Identify the blood parasite species.
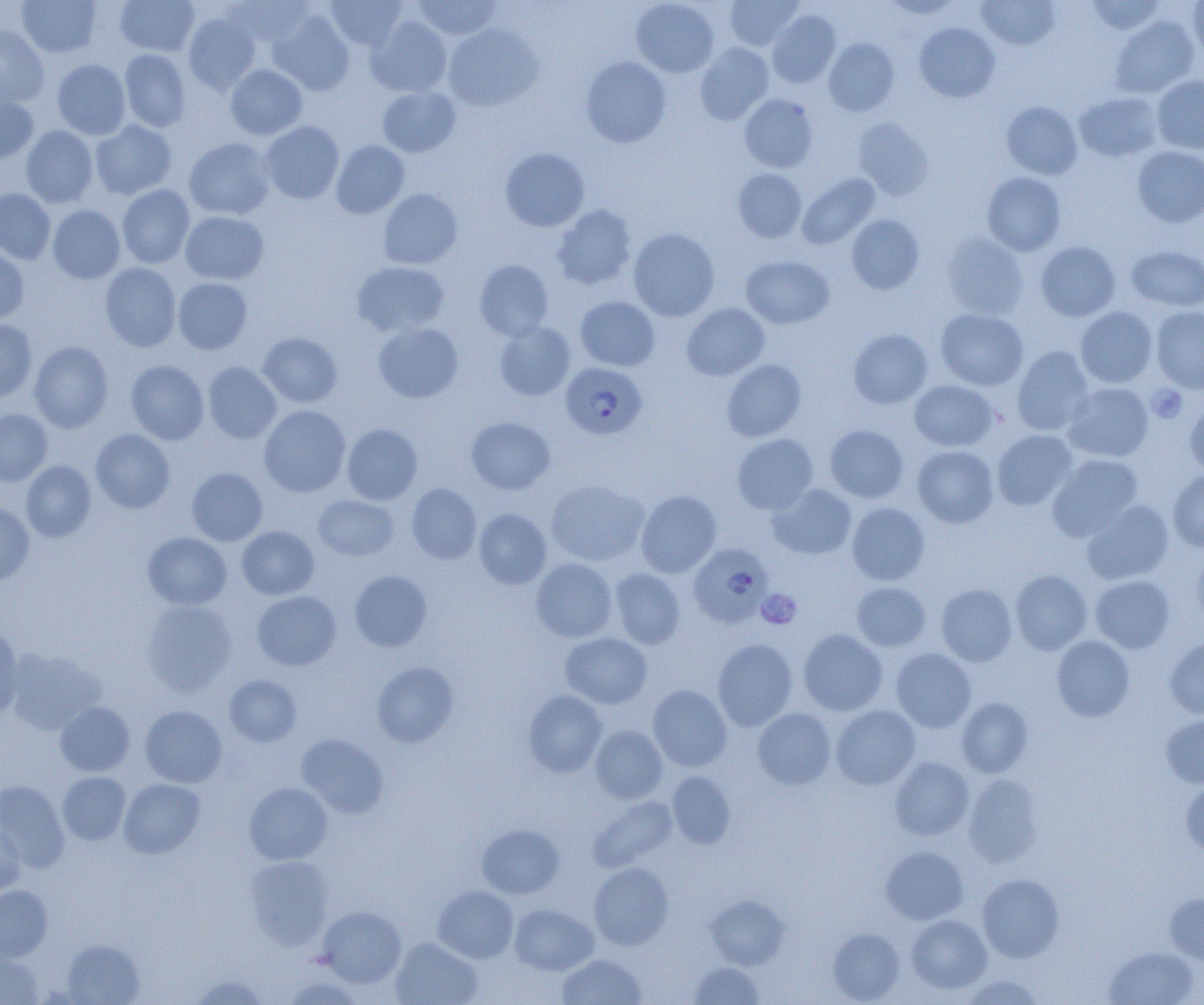
Plasmodium falciparum.

Approximate bounding boxes as (x1, y1, x2, y2) in pixels. Platelet locations: (1147, 384, 1187, 423), (757, 589, 802, 629). Plasmodium falciparum-infected red blood cell locations: (560, 362, 647, 439), (689, 543, 772, 627). Uninfected red blood cell locations: (17, 0, 101, 58), (115, 0, 199, 57), (225, 0, 313, 47), (325, 0, 408, 51), (631, 0, 719, 78), (724, 0, 804, 51), (1085, 0, 1168, 37), (1188, 0, 1204, 61), (413, 1, 503, 40), (882, 1, 964, 19), (976, 1, 1060, 50), (268, 9, 354, 96), (767, 10, 841, 87), (182, 13, 261, 94), (1109, 15, 1200, 99), (367, 16, 452, 97), (914, 22, 1000, 102), (443, 23, 543, 111), (0, 26, 49, 107), (824, 37, 899, 116), (694, 42, 774, 125), (119, 49, 191, 132), (581, 57, 671, 147), (52, 59, 131, 140), (225, 64, 307, 140), (1152, 75, 1204, 155), (377, 86, 460, 157), (1074, 91, 1165, 163), (0, 93, 38, 163), (740, 93, 818, 172), (1001, 101, 1083, 179), (852, 118, 934, 200), (90, 120, 177, 200), (259, 121, 344, 204), (21, 125, 98, 208), (183, 137, 275, 220), (331, 140, 409, 218), (1132, 146, 1204, 227), (500, 148, 590, 231), (733, 168, 806, 242), (982, 172, 1065, 255), (797, 174, 880, 249), (117, 184, 195, 268), (0, 188, 55, 264), (378, 188, 462, 270), (552, 204, 637, 290), (47, 205, 125, 284), (180, 211, 269, 285), (846, 214, 924, 294), (628, 228, 720, 321), (941, 232, 1029, 320), (1035, 241, 1121, 322), (0, 245, 30, 324), (1126, 245, 1204, 311), (741, 255, 834, 328), (475, 259, 553, 341), (352, 261, 449, 337), (100, 263, 181, 352), (173, 278, 252, 354), (575, 296, 660, 371), (682, 303, 769, 381), (1075, 306, 1158, 388), (1151, 306, 1204, 393), (935, 308, 1028, 391), (0, 319, 37, 402), (373, 322, 463, 403), (494, 323, 575, 401), (848, 329, 933, 409), (258, 333, 342, 407), (29, 341, 113, 432), (1012, 346, 1094, 435), (722, 359, 806, 442), (126, 360, 209, 445), (202, 361, 282, 444), (908, 380, 998, 452), (1063, 382, 1154, 462), (1184, 398, 1204, 478), (259, 405, 351, 497), (0, 408, 52, 486), (466, 417, 555, 494), (342, 423, 422, 505), (825, 425, 908, 503), (91, 428, 175, 513), (992, 430, 1077, 510), (733, 434, 818, 514), (912, 446, 998, 528), (1046, 454, 1143, 541), (21, 460, 96, 542), (187, 468, 267, 546), (1167, 470, 1204, 552), (546, 479, 649, 566), (407, 483, 482, 564), (768, 483, 857, 560), (636, 490, 721, 577), (313, 494, 399, 560), (1081, 499, 1174, 585), (0, 502, 35, 586), (846, 502, 930, 585), (473, 509, 552, 589), (236, 526, 319, 599), (143, 532, 232, 609), (1191, 547, 1204, 631), (530, 558, 617, 643), (609, 568, 685, 649), (349, 570, 432, 651), (1010, 570, 1092, 655), (1090, 575, 1175, 653), (851, 582, 932, 652), (936, 584, 1018, 667), (252, 591, 340, 670), (142, 600, 237, 696), (0, 623, 24, 720), (798, 629, 888, 716), (559, 632, 652, 709), (1052, 635, 1135, 722), (712, 638, 797, 731), (1164, 638, 1204, 719), (5, 648, 105, 734), (891, 648, 976, 732), (372, 661, 458, 747), (224, 675, 302, 746), (648, 685, 732, 771), (523, 690, 607, 777), (956, 697, 1033, 778), (55, 702, 134, 776), (140, 705, 227, 788), (830, 705, 921, 790), (752, 707, 836, 789), (1160, 714, 1204, 789), (590, 725, 667, 804), (296, 733, 388, 818), (890, 756, 974, 840), (57, 771, 131, 846), (666, 771, 736, 849), (963, 774, 1044, 867), (119, 778, 205, 859), (1180, 779, 1204, 855), (0, 780, 70, 872), (244, 782, 333, 865), (588, 795, 678, 871), (0, 818, 24, 898), (476, 823, 565, 899), (880, 845, 968, 924), (244, 855, 334, 950), (589, 862, 674, 950), (976, 873, 1064, 962), (0, 885, 52, 962), (433, 886, 518, 963), (1164, 893, 1204, 967), (705, 894, 790, 969), (510, 903, 598, 975), (317, 905, 406, 988), (906, 913, 992, 994), (828, 927, 905, 1003), (390, 937, 482, 1005), (61, 939, 145, 1005), (1104, 946, 1199, 1004), (0, 951, 42, 1004), (556, 953, 647, 1005), (689, 961, 765, 1004), (960, 974, 1046, 1005), (192, 975, 268, 1004), (282, 976, 366, 1005). Captured at 1000x magnification. Thin blood film. One field of a larger specimen. Optical microscopy. Image is 1204×1005 pixels.